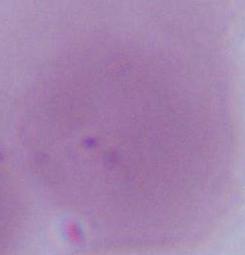

Summary:
  - Identification: red blood cell
  - Modality: photomicrograph
  - Magnification: 1000x